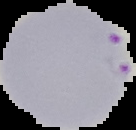

Summary:
  - Malaria status: parasitized
  - Image type: cell region segmented out of the field of view; surrounding area masked to black
  - Image size: 136×130 pixels
  - Preparation: thin blood smear